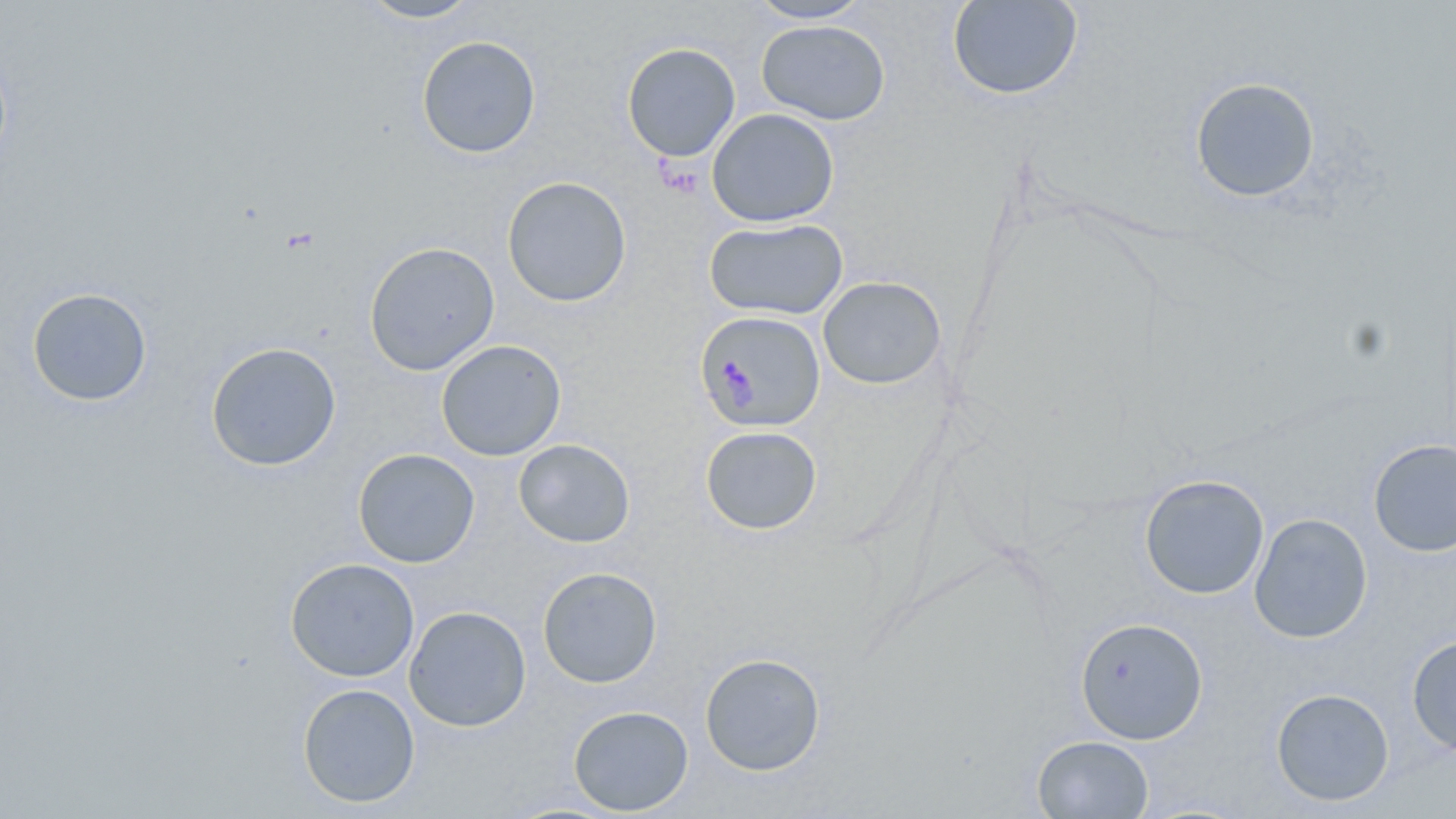

{
  "slide_level_diagnosis": "Plasmodium falciparum",
  "field_of_view": "single",
  "magnification": "1000x",
  "modality": "light microscopy",
  "uninfected_red_blood_cell_locations": "approximate bounding boxes as (x1, y1, x2, y2) in pixels: (357, 0, 482, 23), (947, 0, 1083, 100), (747, 1, 871, 23), (757, 20, 890, 125), (416, 36, 542, 159), (622, 42, 741, 162), (1190, 77, 1320, 202), (707, 108, 839, 227), (502, 176, 632, 307), (704, 217, 849, 320), (363, 241, 500, 376), (818, 276, 946, 389), (26, 287, 153, 407), (435, 340, 567, 461), (205, 341, 341, 472), (700, 425, 822, 534), (1368, 438, 1456, 557), (513, 439, 635, 547), (353, 448, 481, 568), (1139, 474, 1269, 599), (1249, 513, 1373, 643), (285, 557, 420, 682), (537, 567, 663, 688), (404, 606, 531, 732), (1074, 617, 1208, 744), (1406, 634, 1456, 756), (699, 652, 826, 776), (297, 683, 420, 807), (1270, 687, 1395, 806), (568, 705, 694, 816), (1032, 735, 1154, 818)",
  "plasmodium_falciparum_infected_red_blood_cell_locations": "approximate bounding boxes as (x1, y1, x2, y2) in pixels: (695, 309, 825, 433)",
  "stain": "May-Grünwald-Giemsa",
  "image_size": "1456×819 pixels",
  "preparation": "thin blood smear"
}